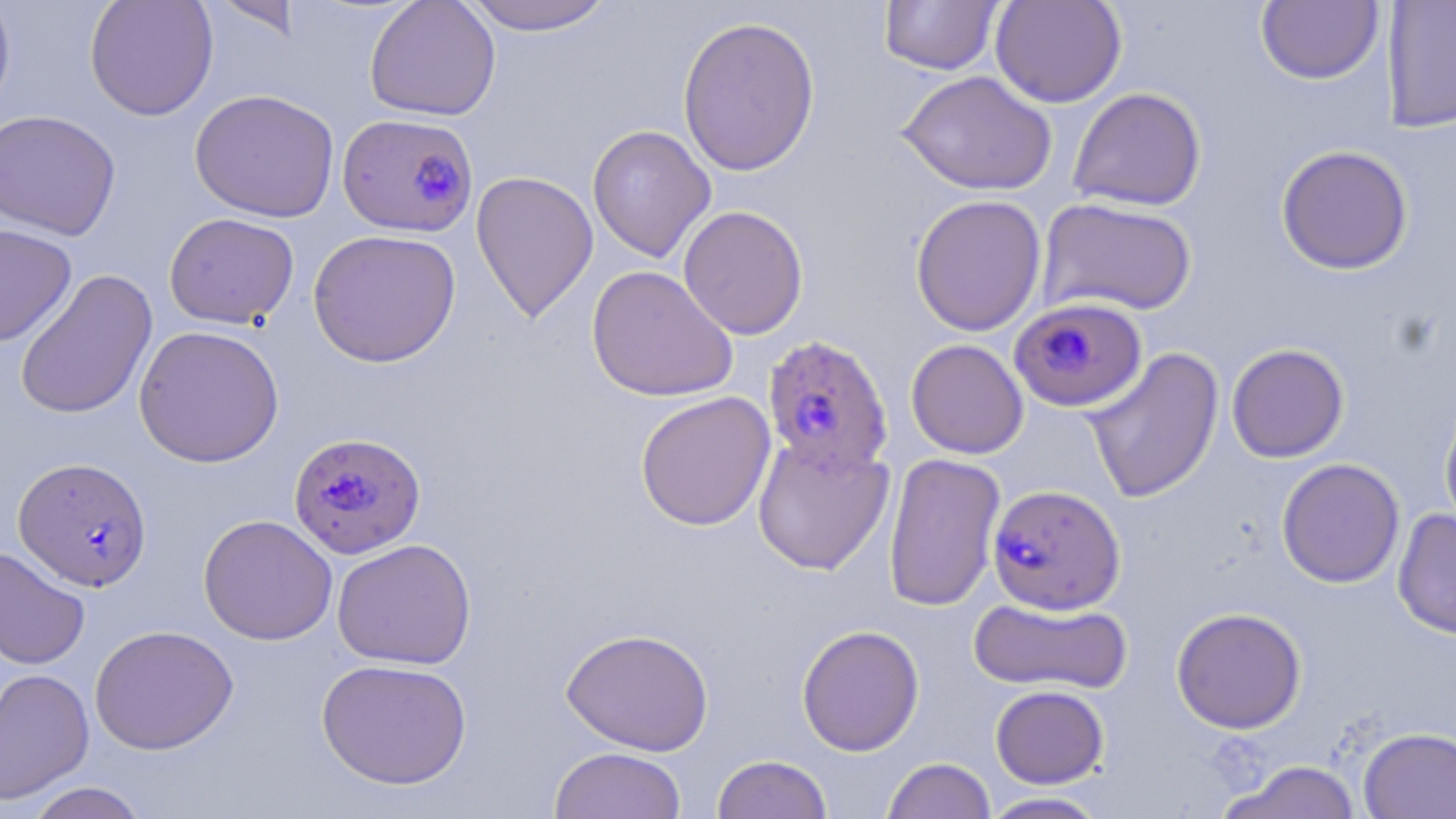 Approximate bounding boxes as (x1, y1, x2, y2) in pixels. Plasmodium falciparum-infected red blood cell locations: (337, 112, 479, 237), (1008, 296, 1147, 416), (762, 334, 893, 476), (288, 432, 426, 559), (13, 457, 152, 592), (987, 483, 1126, 614). Uninfected red blood cell locations: (0, 0, 17, 122), (84, 0, 219, 121), (210, 0, 304, 41), (364, 0, 501, 121), (457, 0, 618, 35), (990, 0, 1127, 108), (879, 1, 1004, 75), (1255, 1, 1384, 85), (1381, 1, 1456, 133), (677, 14, 821, 177), (897, 70, 1057, 196), (1067, 86, 1206, 211), (189, 89, 340, 222), (0, 109, 121, 241), (587, 124, 716, 264), (1275, 144, 1414, 275), (470, 170, 599, 323), (909, 194, 1047, 336), (1037, 197, 1198, 317), (677, 204, 809, 340), (164, 212, 300, 329), (0, 223, 77, 347), (308, 228, 462, 368), (586, 264, 739, 402), (13, 268, 158, 421), (134, 324, 285, 468), (906, 338, 1029, 459), (1226, 343, 1349, 462), (1083, 346, 1224, 504), (635, 391, 776, 532), (1439, 396, 1456, 534), (752, 432, 895, 576), (883, 451, 1005, 613), (1276, 458, 1405, 588), (1392, 509, 1456, 639), (198, 514, 338, 645), (332, 537, 477, 670), (0, 545, 91, 670), (968, 595, 1133, 695), (1171, 607, 1307, 734), (89, 624, 239, 755), (796, 624, 925, 756), (560, 627, 715, 756), (316, 658, 473, 790), (0, 667, 94, 805), (990, 685, 1109, 788), (1358, 727, 1456, 819), (548, 746, 686, 819), (711, 754, 833, 818), (882, 757, 996, 819), (1219, 760, 1364, 818), (23, 782, 150, 819), (977, 792, 1110, 818). Slide-level diagnosis: Plasmodium falciparum. Image is 1456×819 pixels. One field of a larger specimen. Optical microscopy. Thin blood smear. May-Grünwald-Giemsa-stained preparation. Captured at 1000x magnification.